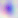 Captured at 400x magnification. Photomicrograph. Toxoplasma gondii is seen.